State which parasite is depicted.
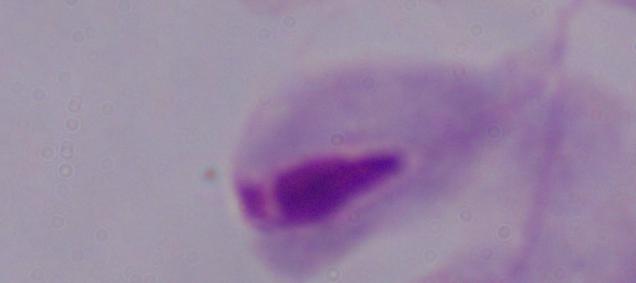
This is a trichomonad.

Captured at 1000x magnification. Micrograph.